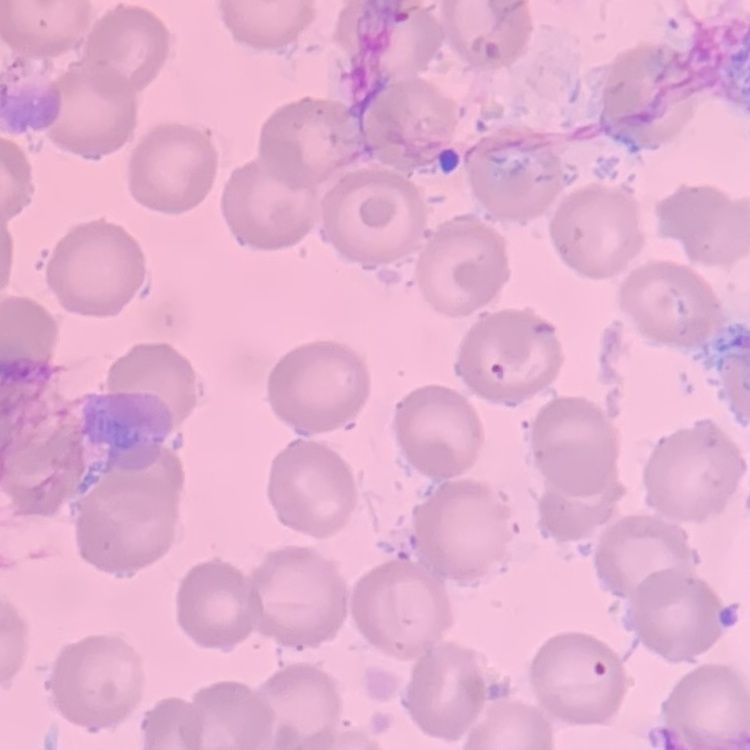
Summary:
  - Erythrocyte morphology: no rouleaux formation
  - Preparation: thin blood smear
  - Image type: one tile cut from a larger photomicrograph
  - Stain: Field's or Giemsa